Report the malaria status of this cell.
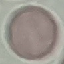

Uninfected.

stain = Giemsa
preparation = thin blood smear
image type = automatically extracted cell patch, resized to 64 × 64 pixels
capture = smartphone through the microscope eyepiece